Name the parasite shown.
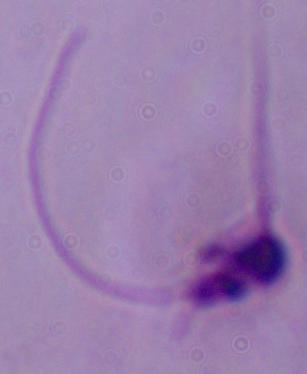

This is Leishmania.

Summary:
  - Magnification: 1000x
  - Modality: micrograph